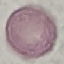

Malaria status: uninfected. Photographed with a smartphone camera at the microscope eyepiece. Cell patch, automatically extracted from a larger field of view and resized to 64 × 64 pixels. Thin smear of blood. Giemsa-stained preparation.